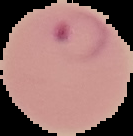
Image is 133×136 pixels. Result: malaria parasites detected. The area outside the segmented cell region is set to black. From a thin blood film.